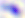

Summary:
  - Identification: Toxoplasma gondii
  - Magnification: 400x
  - Modality: micrograph